Classify this cell by malaria status.
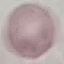

Uninfected.

Automatically extracted cell patch, resized to 64 × 64 pixels. Acquired by smartphone through the microscope eyepiece. Giemsa stain. Thin blood film.